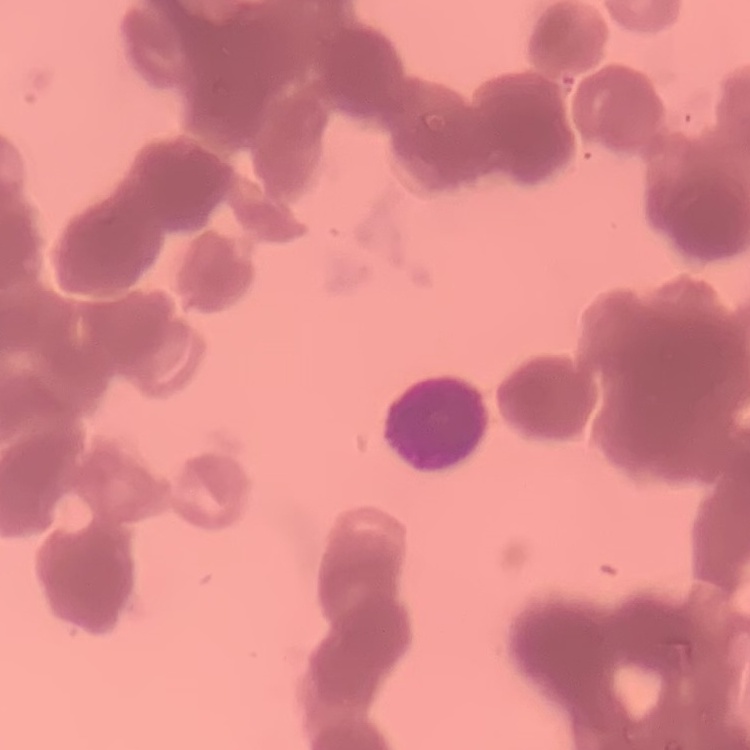
Summary:
  - Red blood cell morphology: rouleaux formation
  - Image type: square crop of a larger photomicrograph
  - Stain: Field's or Giemsa
  - Preparation: thin peripheral smear